Locate every Plasmodium parasite.
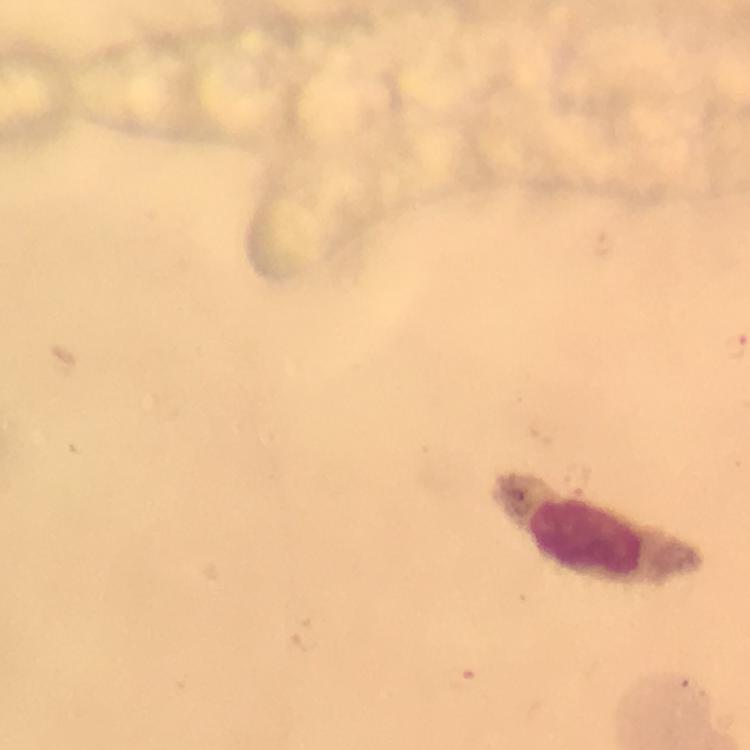

No Plasmodium parasites detected.

stain = Giemsa
preparation = thick smear
context = from a diagnostic examination for malaria
magnification = 100x
immersion oil = applied
leukocyte locations = approximate centers as [x, y] in pixels: [601, 531]
cropped from = one field of view
image size = 750×750 pixels
capture = smartphone camera through the microscope